Locate and identify every blood parasite.
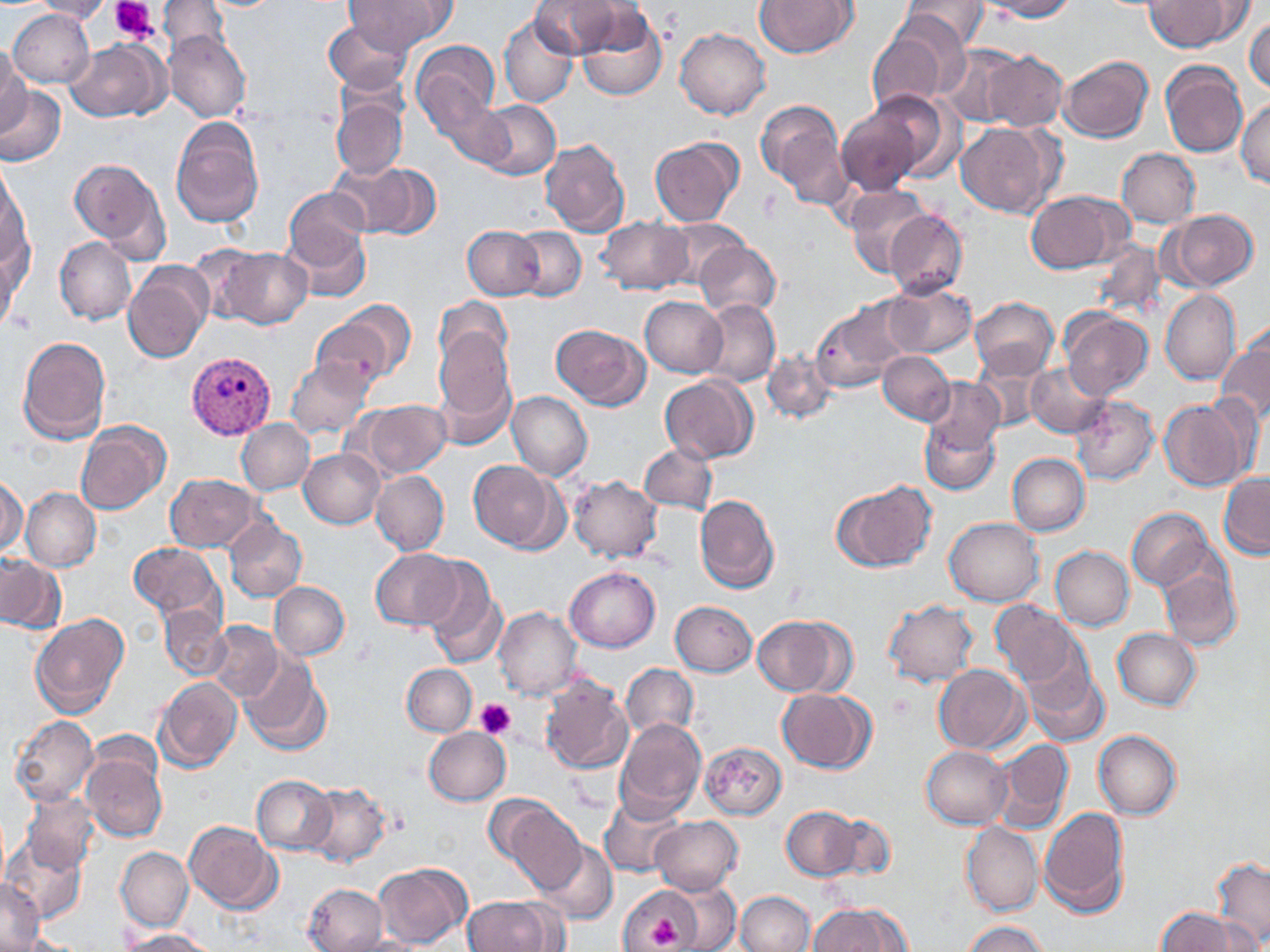

Approximate bounding boxes as (x1,y1)-(x2,y2) corner pairs in pixels.
Plasmodium vivax-infected red blood cells: (186,350)-(276,438).
No Plasmodium falciparum, Plasmodium ovale, Plasmodium malariae, Babesia divergens, or Trypanosoma brucei observed.

Uninfected red blood cell locations: (158,0)-(228,56), (345,0)-(450,53), (530,0)-(626,58), (754,0)-(857,58), (900,0)-(991,51), (974,0)-(1076,20), (1145,0)-(1244,51), (27,1)-(115,22), (576,6)-(668,102), (8,8)-(94,89), (499,15)-(578,108), (1245,15)-(1270,93), (323,18)-(415,93), (865,25)-(960,112), (675,27)-(770,119), (165,31)-(251,122), (411,39)-(502,132), (66,40)-(167,121), (939,44)-(1026,126), (0,48)-(28,134), (979,50)-(1068,132), (1058,56)-(1154,143), (1160,61)-(1247,158), (1,86)-(64,165), (871,91)-(957,182), (331,96)-(407,179), (1236,98)-(1270,188), (435,99)-(514,167), (476,100)-(561,180), (756,100)-(849,207), (835,105)-(926,196), (170,118)-(264,228), (955,122)-(1060,219), (649,138)-(744,226), (540,139)-(630,236), (1117,148)-(1200,228), (69,158)-(169,261), (340,161)-(439,240), (1,167)-(30,273), (845,185)-(935,278), (284,188)-(369,269), (1025,189)-(1131,274), (882,208)-(967,297), (1164,209)-(1259,291), (596,217)-(694,293), (658,219)-(745,288), (286,222)-(371,304), (463,225)-(543,300), (511,226)-(587,301), (1,234)-(30,325), (55,237)-(135,325), (695,241)-(781,318), (1092,241)-(1165,320), (215,247)-(312,329), (0,250)-(18,338), (123,262)-(212,363), (883,282)-(977,358), (1161,289)-(1242,385), (641,296)-(728,377), (434,297)-(513,371), (967,297)-(1058,377), (700,298)-(781,388), (329,300)-(416,383), (811,301)-(907,391), (1060,310)-(1153,401), (311,319)-(392,390), (551,324)-(650,410), (434,328)-(515,422), (1216,333)-(1270,425), (17,335)-(111,444), (761,350)-(837,424), (877,350)-(954,424), (973,352)-(1051,431), (286,357)-(374,439), (1026,362)-(1109,436), (659,375)-(757,463), (922,375)-(1004,454), (507,392)-(593,479), (1071,397)-(1158,485), (1158,398)-(1250,491), (359,400)-(452,478), (919,418)-(1001,496), (235,419)-(314,495), (75,421)-(170,515), (639,444)-(717,515), (298,448)-(384,529), (1008,453)-(1090,536), (467,460)-(563,553), (371,469)-(449,555), (1219,473)-(1269,558), (164,474)-(261,552), (568,474)-(662,563), (1,477)-(27,556), (831,479)-(938,574), (20,487)-(100,571), (695,495)-(779,594), (1127,508)-(1213,589), (944,517)-(1044,606), (224,520)-(306,602), (128,541)-(224,623), (1050,546)-(1134,631), (370,549)-(461,630), (0,556)-(65,633), (1158,563)-(1242,652), (421,565)-(506,671), (564,567)-(659,651), (270,582)-(349,660), (883,599)-(977,686), (670,600)-(756,676), (991,600)-(1079,687), (158,605)-(230,679), (494,607)-(582,701), (30,615)-(128,717), (752,615)-(846,696), (206,622)-(284,701), (1112,628)-(1200,710), (239,654)-(331,755), (1021,659)-(1109,746), (620,663)-(698,741), (402,664)-(477,735), (931,665)-(1027,753), (154,676)-(242,772), (538,676)-(634,775), (777,688)-(874,772), (9,714)-(99,805), (615,718)-(706,818), (422,727)-(510,806), (1093,730)-(1182,820), (991,738)-(1073,835), (700,742)-(786,819), (921,746)-(1013,830), (82,749)-(167,841), (252,775)-(337,854), (302,783)-(391,865), (21,792)-(101,874), (600,796)-(684,877), (497,802)-(587,894), (782,806)-(859,880), (1039,807)-(1130,917), (824,813)-(897,881), (650,816)-(742,894), (186,820)-(281,912), (962,822)-(1044,916), (2,838)-(85,925), (535,840)-(617,924), (116,846)-(193,931), (1211,857)-(1269,948), (373,862)-(471,948), (0,881)-(45,949), (303,884)-(388,951), (619,886)-(730,946), (735,891)-(814,952), (462,895)-(559,951), (809,903)-(909,951), (1155,908)-(1251,952), (961,921)-(1050,952), (120,928)-(216,951), (14,933)-(82,952). Platelet locations: (111,0)-(156,41), (887,692)-(915,722), (475,698)-(516,740), (641,913)-(686,949). Slide-level diagnosis: Plasmodium vivax. One field of a larger specimen. May-Grünwald-Giemsa stain. Optical microscopy. Image is 1270×952 pixels. 1000x magnification. Thin blood film.